State which parasite is depicted.
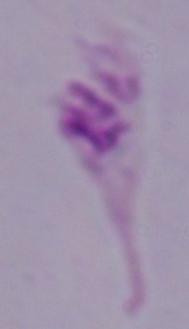

This is Leishmania.

magnification = 1000x
modality = micrograph